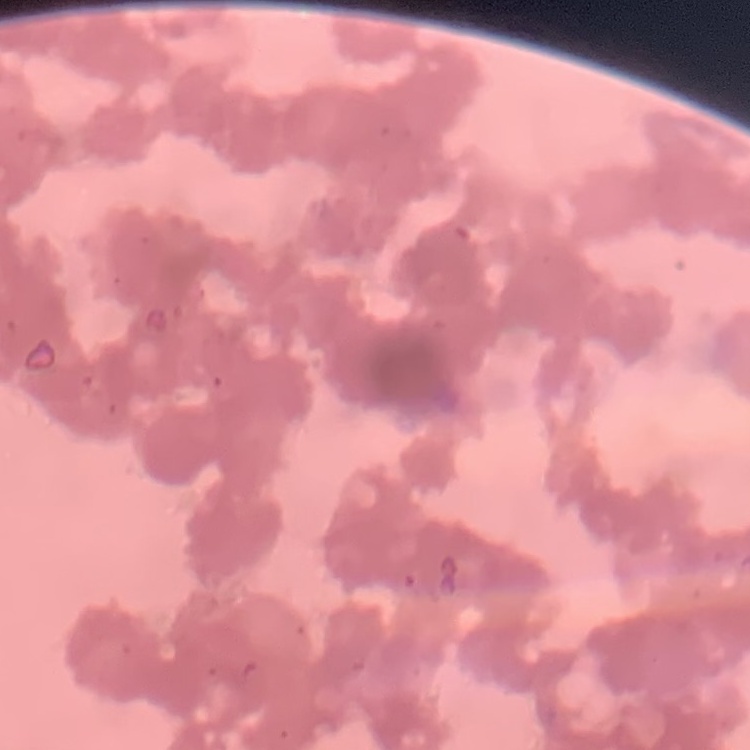
Summary:
  - Red blood cell morphology: rouleaux formation
  - Preparation: thin blood film
  - Image type: one tile cut from a larger photomicrograph
  - Stain: Field's or Giemsa